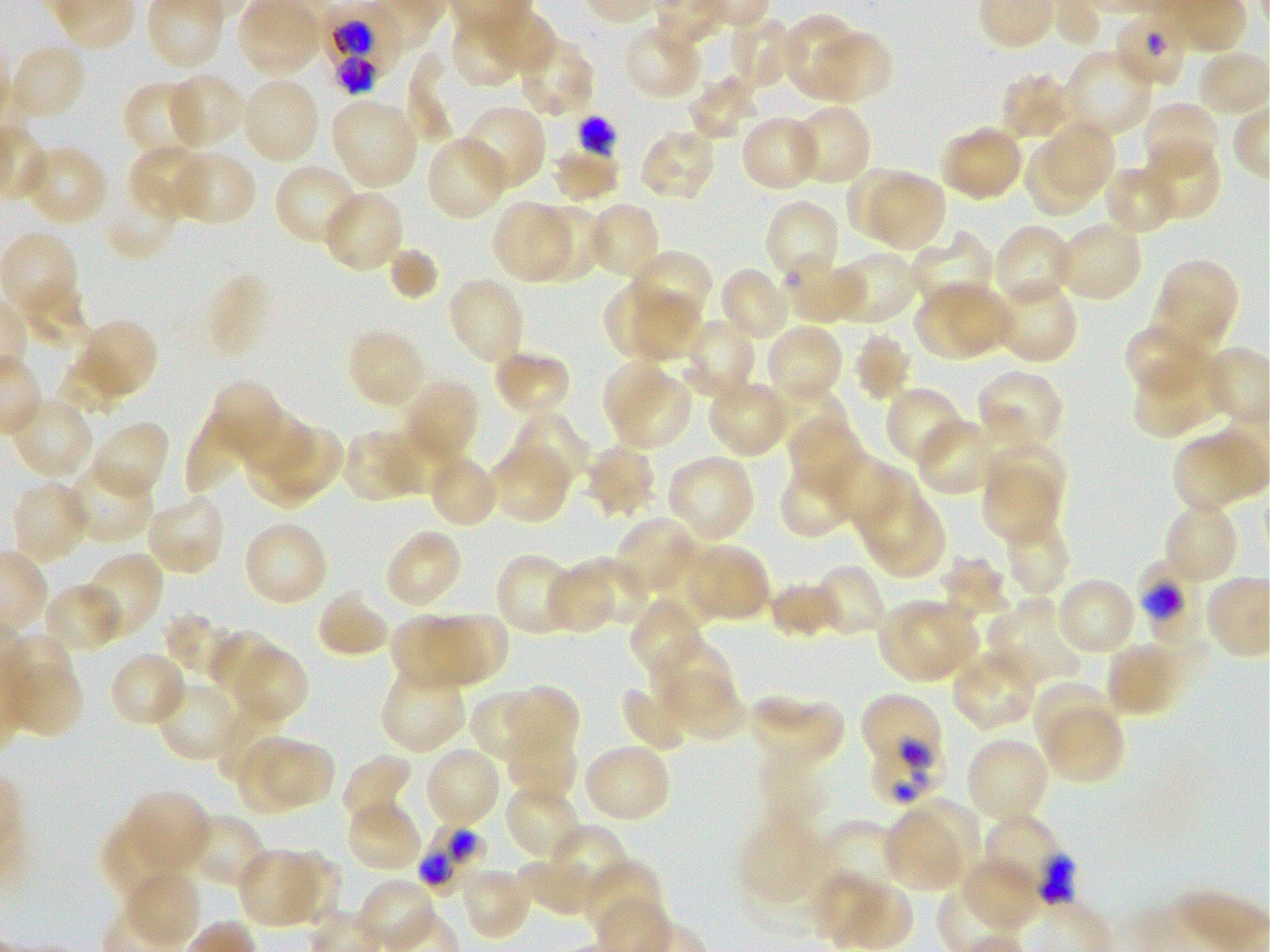
Not every red blood cell is marked. A life-cycle stage — or a range of stages, where the recorded stages span more than one — follows each staged infected red blood cell.
locations_of_uninfected_red_blood_cells: 'approximate bounding boxes as (x1, y1, x2, y2) in pixels: (485, 8, 557, 68), (780, 14, 859, 98), (728, 15, 795, 92), (623, 21, 705, 100), (449, 22, 516, 86), (813, 35, 893, 103), (521, 38, 592, 115), (10, 42, 89, 120), (1066, 48, 1154, 136), (409, 49, 459, 144), (164, 72, 245, 152), (1001, 72, 1075, 141), (689, 73, 758, 141), (239, 76, 320, 165), (122, 80, 203, 158), (329, 95, 419, 191), (1142, 100, 1221, 181), (791, 104, 873, 182), (461, 109, 545, 189), (740, 115, 822, 193), (1043, 120, 1116, 197), (940, 124, 1024, 202), (637, 127, 717, 202), (424, 136, 509, 221), (1024, 140, 1099, 217), (1144, 141, 1221, 222), (23, 144, 108, 227), (127, 145, 213, 221), (551, 148, 619, 204), (170, 150, 256, 227), (273, 163, 363, 247), (1103, 164, 1179, 235), (847, 167, 922, 239), (872, 175, 946, 251), (106, 176, 180, 258), (322, 190, 404, 274), (764, 199, 841, 289), (490, 201, 575, 284), (593, 202, 660, 277), (530, 203, 605, 281), (1055, 219, 1144, 302), (992, 223, 1074, 308), (910, 233, 995, 311), (388, 247, 438, 301), (827, 250, 919, 327), (631, 252, 711, 320), (1164, 258, 1239, 333), (783, 259, 865, 326), (720, 265, 793, 344), (20, 271, 91, 350), (446, 277, 525, 367), (991, 278, 1078, 364), (914, 281, 1013, 361), (603, 283, 697, 361), (1149, 286, 1224, 358), (633, 291, 703, 361), (684, 318, 756, 396), (85, 323, 156, 392), (764, 323, 844, 405), (346, 327, 428, 410), (853, 331, 912, 401), (1125, 331, 1205, 394), (492, 349, 572, 418), (55, 353, 129, 416), (1133, 356, 1231, 439), (605, 357, 666, 434), (978, 369, 1063, 442), (617, 377, 693, 451), (708, 379, 790, 458), (407, 381, 477, 454), (214, 383, 276, 455), (884, 385, 966, 468), (768, 387, 845, 452), (15, 400, 89, 476), (237, 405, 312, 475), (188, 409, 245, 492), (506, 410, 589, 490), (786, 415, 864, 494), (915, 418, 995, 496), (89, 420, 171, 502), (272, 425, 343, 492), (384, 429, 463, 496), (344, 431, 413, 501), (245, 438, 323, 510), (1172, 439, 1240, 515), (490, 442, 573, 524), (584, 442, 657, 518), (991, 443, 1066, 514), (665, 452, 756, 544), (826, 452, 899, 532), (434, 456, 495, 523), (778, 461, 858, 537), (67, 463, 155, 544), (855, 467, 927, 553), (982, 471, 1056, 543), (10, 480, 91, 566), (144, 492, 226, 577), (873, 497, 944, 579), (1163, 501, 1240, 586), (614, 516, 691, 595), (1003, 519, 1070, 598), (242, 521, 329, 607), (384, 527, 463, 611), (656, 543, 721, 629), (688, 547, 767, 617), (79, 552, 163, 643), (496, 553, 580, 636), (573, 554, 649, 625), (941, 556, 1008, 616), (813, 564, 887, 637), (549, 569, 611, 632), (1055, 576, 1138, 657), (767, 581, 841, 639), (41, 582, 123, 655), (316, 588, 391, 659), (629, 596, 705, 680), (877, 597, 979, 684), (988, 597, 1082, 689), (164, 611, 243, 683), (392, 613, 456, 687), (424, 613, 508, 685), (208, 631, 282, 707), (650, 637, 731, 713), (1105, 641, 1186, 717), (229, 643, 307, 727), (951, 648, 1038, 732), (108, 651, 189, 728), (8, 658, 82, 738), (380, 664, 466, 754), (661, 671, 748, 743), (155, 678, 245, 762), (1032, 680, 1109, 764), (620, 685, 695, 754), (504, 688, 578, 759), (215, 693, 282, 781), (470, 693, 536, 766), (746, 694, 845, 770), (1043, 707, 1124, 785), (504, 725, 578, 802), (235, 735, 304, 815), (965, 736, 1050, 826), (265, 741, 335, 804), (581, 742, 672, 823), (423, 745, 501, 830), (342, 754, 412, 829), (504, 782, 583, 861), (122, 790, 211, 875), (908, 795, 980, 881), (345, 798, 423, 874), (883, 811, 962, 894), (184, 813, 267, 890), (742, 819, 825, 901), (102, 820, 185, 906), (821, 821, 897, 897), (538, 824, 629, 912), (237, 848, 327, 928), (287, 852, 342, 925), (959, 857, 1043, 933), (517, 859, 600, 917), (580, 859, 665, 937), (458, 866, 533, 941), (123, 872, 201, 949), (818, 874, 879, 948), (854, 879, 914, 951)'
donor_blood_group: O+
field_of_view: single
culture: in-vitro Plasmodium falciparum strain 3D7, static
objective: 100x, oil immersion, numerical aperture 1.25
preparation: thin blood smear
locations_of_red_blood_cells_of_indeterminate_infection_status: 'approximate bounding boxes as (x1, y1, x2, y2) in pixels: (577, 116, 614, 158), (869, 749, 947, 805), (981, 814, 1073, 905)'
locations_of_infected_red_blood_cells: 'approximate bounding boxes as (x1, y1, x2, y2) in pixels: (318, 0, 402, 93); (1113, 9, 1189, 90); (1137, 558, 1205, 643) early trophozoite; (860, 693, 941, 766) early trophozoite; (419, 822, 489, 897)'
stain: Giemsa
image_size: 1270×952 pixels